Locate every leukocyte (white blood cell).
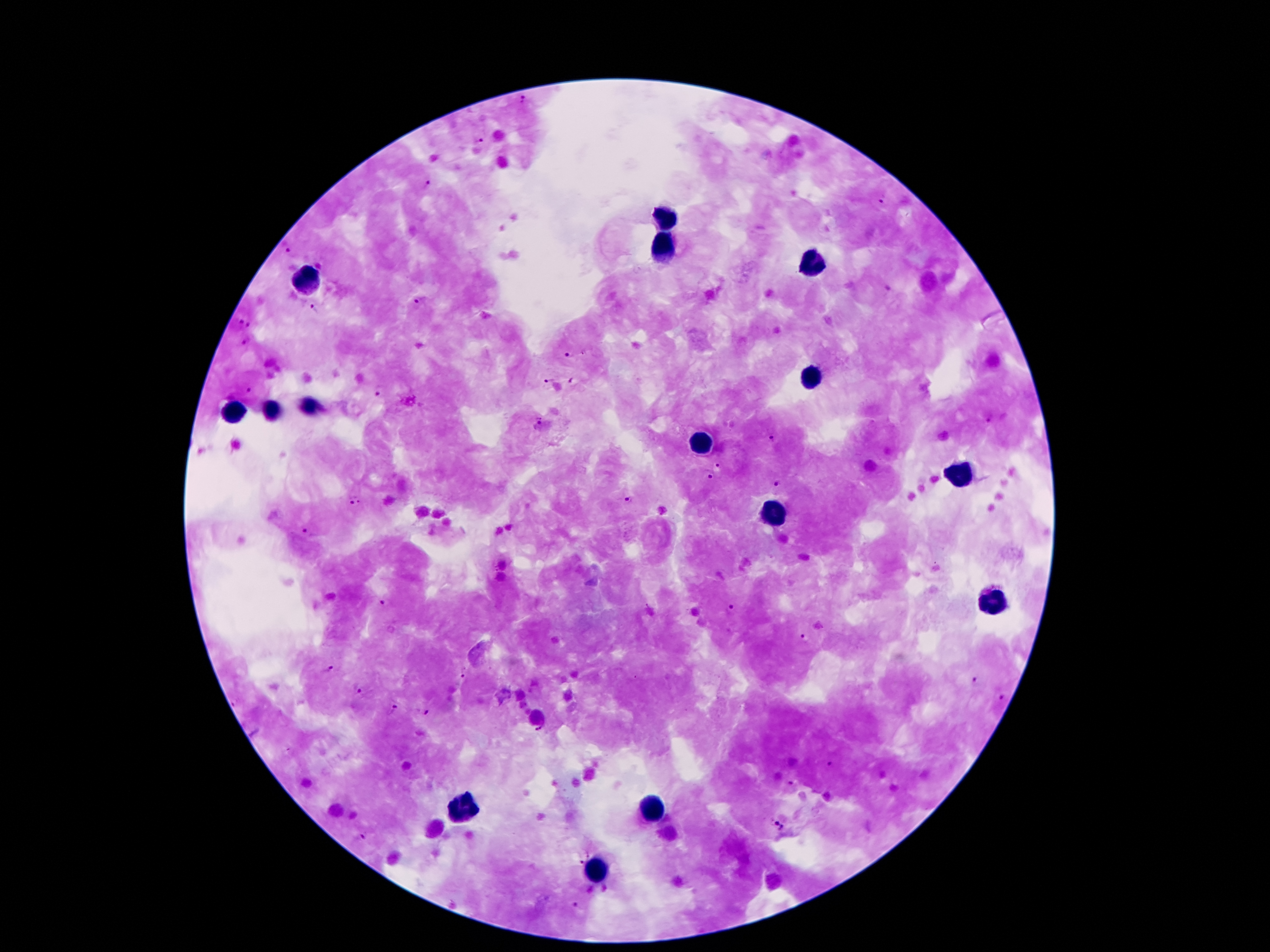

Approximate object centers, in pixels from the top-left corner.
Leukocytes: (x=667, y=218), (x=665, y=248), (x=812, y=265), (x=302, y=286), (x=810, y=376), (x=310, y=404), (x=268, y=408), (x=232, y=412), (x=699, y=443), (x=961, y=472), (x=775, y=512), (x=993, y=599), (x=464, y=806), (x=651, y=813), (x=596, y=876).

Malaria parasite locations: (x=523, y=101), (x=479, y=142), (x=428, y=185), (x=880, y=199), (x=285, y=249), (x=419, y=301), (x=318, y=310), (x=240, y=322), (x=249, y=324), (x=247, y=341), (x=568, y=352), (x=548, y=380), (x=572, y=380), (x=382, y=389), (x=249, y=391), (x=989, y=418), (x=539, y=424), (x=770, y=437), (x=715, y=465), (x=710, y=476), (x=779, y=482), (x=628, y=501), (x=356, y=503), (x=309, y=532), (x=383, y=603), (x=732, y=611), (x=805, y=640), (x=329, y=670), (x=465, y=673), (x=975, y=681), (x=362, y=690), (x=998, y=698), (x=392, y=708), (x=425, y=711), (x=540, y=730), (x=829, y=763), (x=791, y=783), (x=780, y=827), (x=362, y=837), (x=579, y=862), (x=578, y=906). Patient malaria status: positive for Plasmodium falciparum. 100x magnification. Single field of view. Photographed through the microscope eyepiece with a smartphone camera. Image is 1270×952 pixels. Giemsa-stained preparation. Thick blood film.